Name the parasite shown.
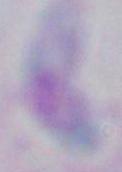

This is Toxoplasma gondii.

magnification = 1000x
modality = photomicrograph